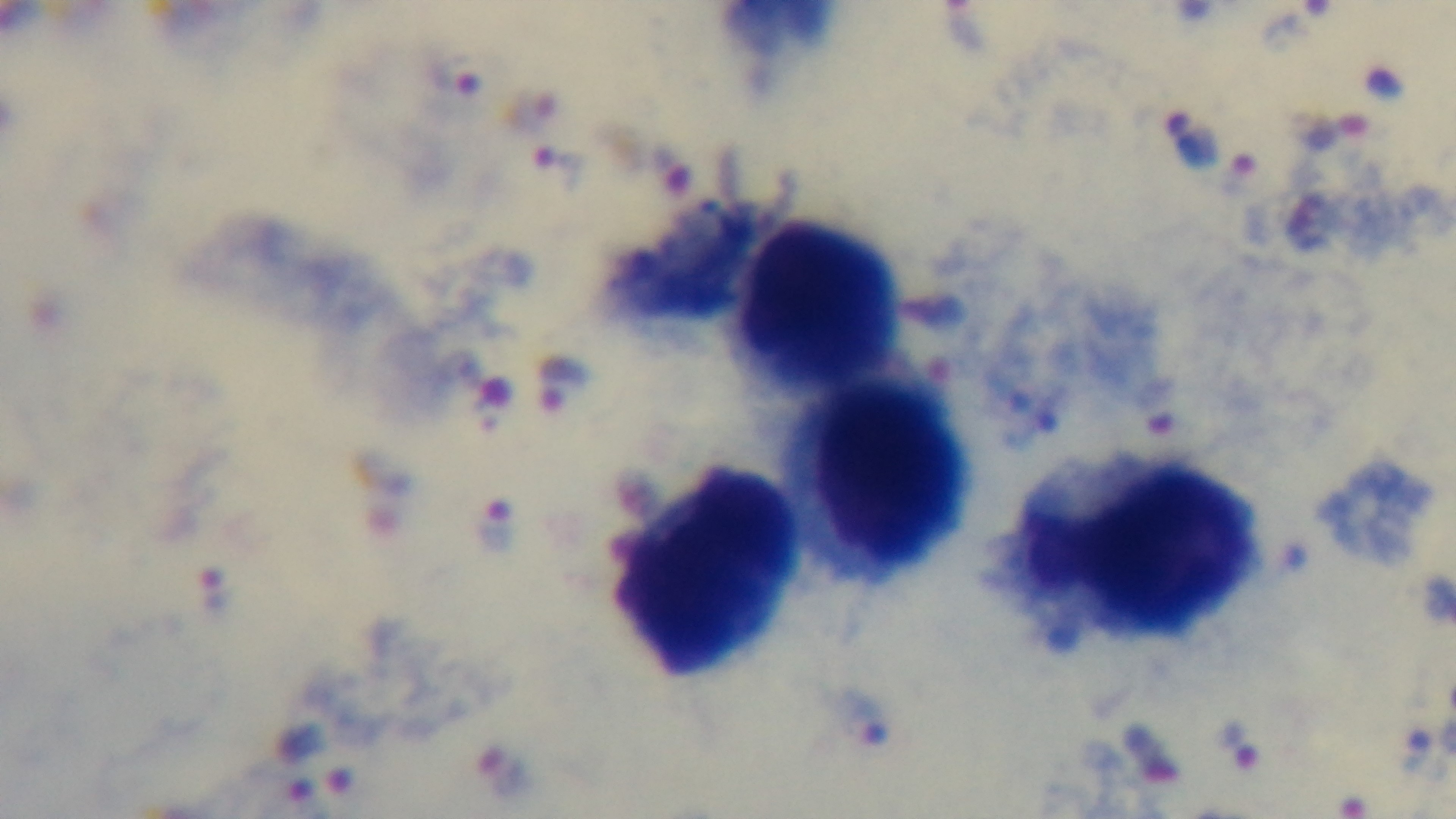

Summary:
  - Malaria status: infected
  - Modality: light microscopy
  - Preparation: thick blood film
  - Objective: 100x oil immersion
  - Field of view: one from the slide
  - Capture: mounted 4K digital camera
  - Stain: Giemsa